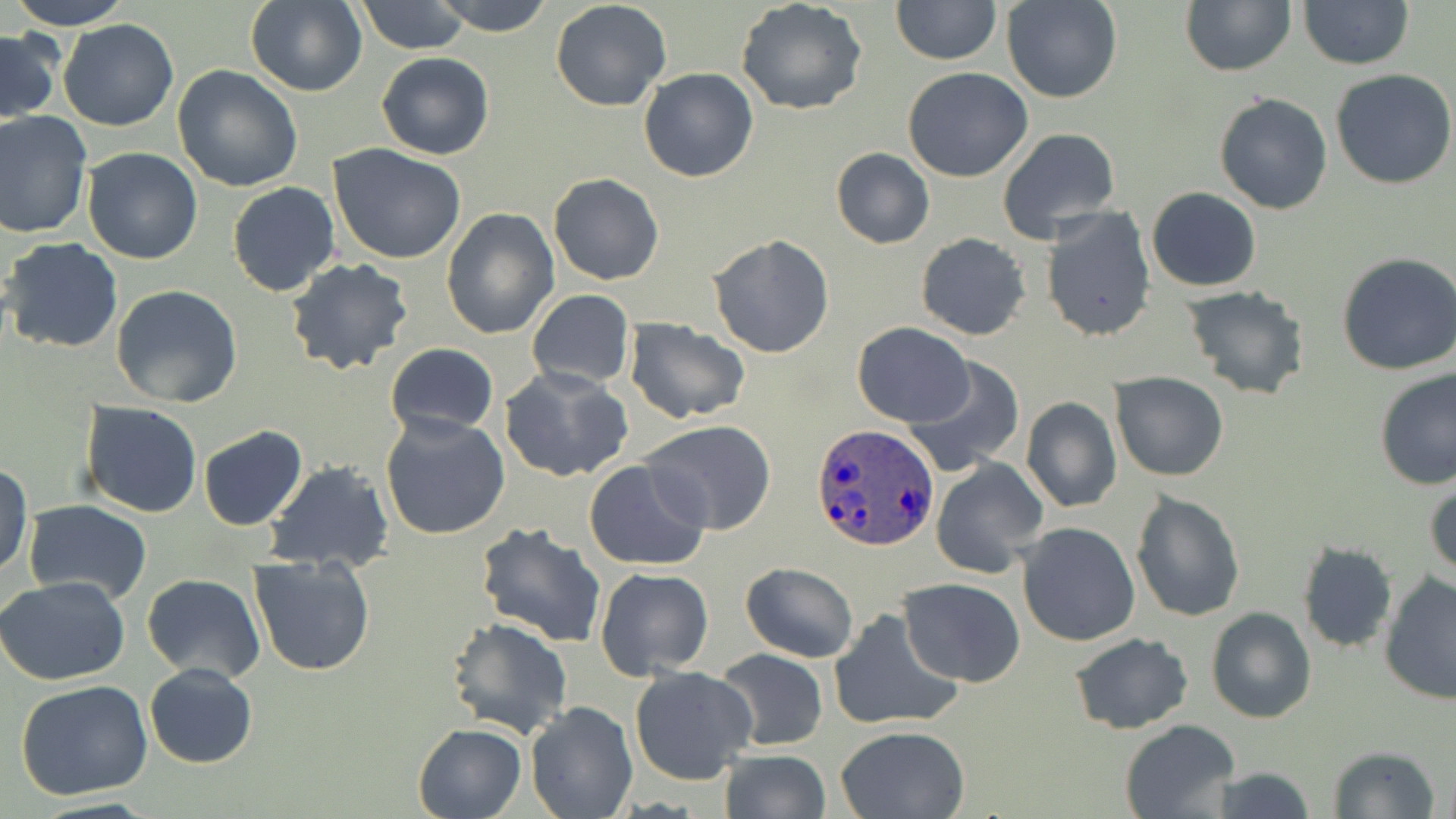

slide-level diagnosis = Plasmodium ovale
preparation = thin blood film
modality = optical microscopy
magnification = 1000x
image size = 1456×819 pixels
stain = May-Grünwald-Giemsa
field of view = one of a larger specimen
Plasmodium ovale-infected red blood cell locations = approximate bounding boxes as (x1,y1)-(x2,y2) corner pairs in pixels: (812,421)-(940,551)
uninfected red blood cell locations = approximate bounding boxes as (x1,y1)-(x2,y2) corner pairs in pixels: (9,0)-(134,29), (356,0)-(472,54), (433,0)-(556,35), (891,0)-(1001,65), (1003,0)-(1122,103), (1180,0)-(1296,76), (245,1)-(367,97), (550,1)-(672,113), (736,1)-(868,116), (1298,1)-(1414,70), (59,18)-(178,131), (1,28)-(60,126), (375,51)-(494,159), (173,64)-(305,192), (639,67)-(759,183), (903,67)-(1033,182), (1329,67)-(1456,190), (1214,91)-(1334,215), (0,111)-(94,239), (996,126)-(1122,243), (328,144)-(469,265), (80,147)-(203,264), (831,147)-(933,248), (260,163)-(448,287), (548,173)-(664,285), (227,181)-(340,297), (1146,187)-(1262,292), (1041,206)-(1155,343), (440,209)-(558,339), (915,232)-(1032,340), (708,234)-(836,357), (1,237)-(123,353), (1337,250)-(1456,377), (285,257)-(412,375), (110,285)-(243,407), (1182,286)-(1311,400), (527,289)-(634,390), (624,318)-(750,424), (852,324)-(974,427), (385,343)-(499,437), (902,359)-(1025,479), (500,366)-(633,483), (1375,366)-(1456,490), (1112,373)-(1227,481), (1020,397)-(1123,513), (78,401)-(203,520), (380,412)-(511,539), (640,419)-(780,536), (197,425)-(308,531), (930,457)-(1047,577), (264,460)-(395,574), (584,460)-(710,570), (0,463)-(33,580), (1425,472)-(1456,583), (1129,489)-(1246,623), (22,500)-(151,603), (473,520)-(607,647), (1016,521)-(1142,647), (1296,542)-(1399,654), (248,554)-(378,677), (740,562)-(859,663), (594,567)-(714,679), (141,573)-(266,683), (1379,573)-(1456,704), (0,577)-(130,686), (899,577)-(1025,687), (1205,607)-(1317,725), (829,608)-(963,732), (445,617)-(574,740), (1069,631)-(1193,735), (714,647)-(829,750), (144,663)-(258,769), (628,665)-(759,786), (15,680)-(155,802), (525,700)-(638,818), (1119,720)-(1241,818), (412,723)-(526,819), (835,725)-(969,818), (1327,746)-(1441,818), (717,749)-(832,819), (1205,767)-(1316,819)